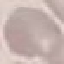
Malaria status: uninfected. Acquired by smartphone through the microscope eyepiece. Cell patch, automatically extracted from a larger field of view and resized to 64 × 64 pixels. Giemsa stain. Thin smear of blood.